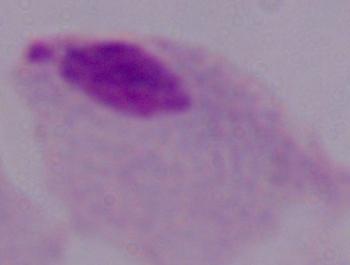 A trichomonad is seen. Photomicrograph. Captured at 1000x magnification.